Give the extent of all Plasmodium malariae-infected red blood cells.
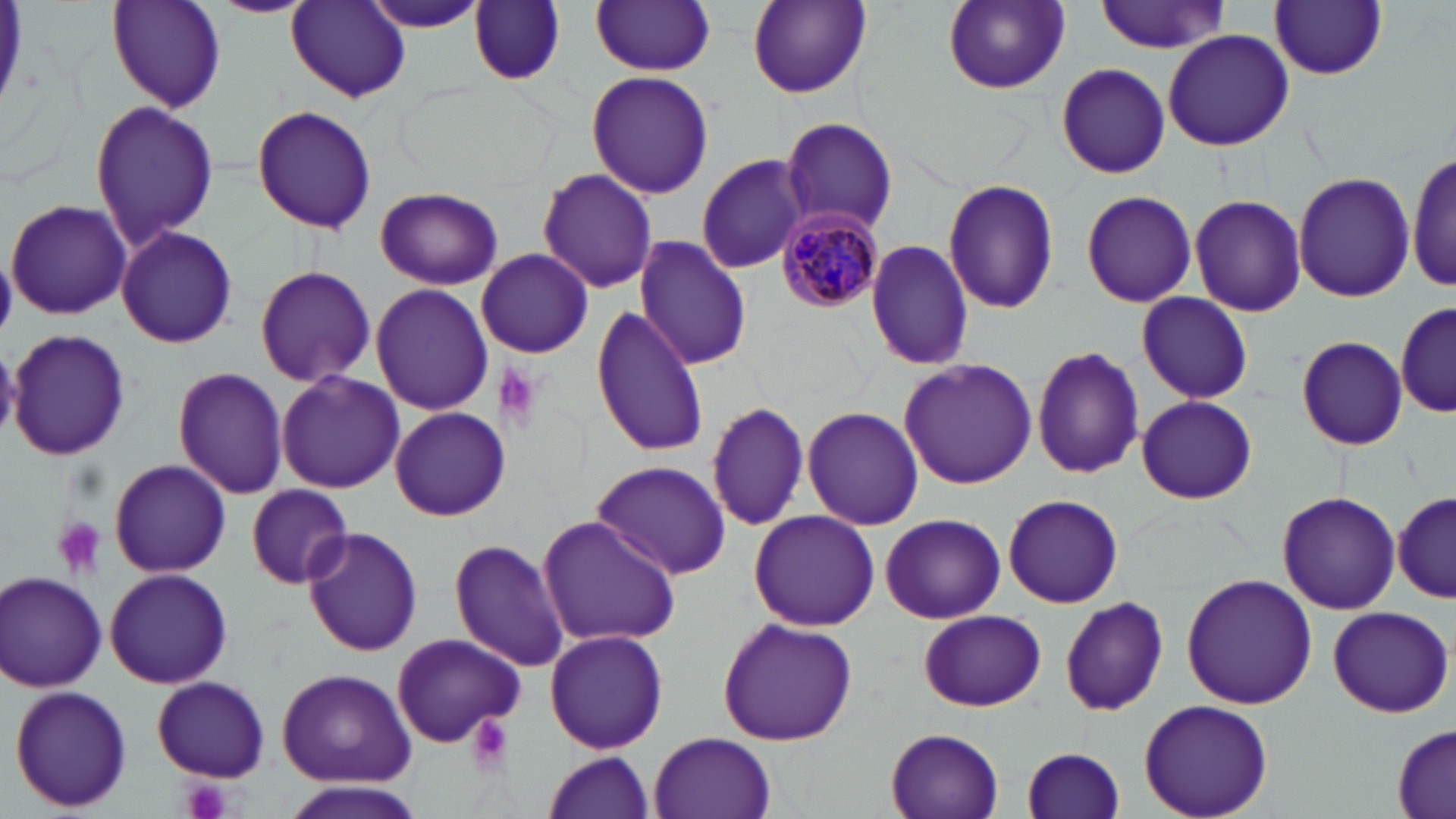
Approximate bounding boxes as [x1, y1, x2, y2] in pixels.
Plasmodium malariae-infected red blood cells: [774, 203, 886, 314].

Platelet locations: [491, 365, 545, 431], [52, 518, 106, 579], [466, 715, 513, 777], [179, 777, 232, 819]. Uninfected red blood cell locations: [207, 0, 317, 18], [942, 0, 1069, 93], [107, 1, 226, 112], [285, 1, 410, 104], [358, 1, 489, 33], [468, 1, 566, 86], [746, 1, 870, 98], [1093, 1, 1232, 54], [591, 2, 718, 75], [1271, 2, 1388, 80], [1162, 29, 1294, 153], [1057, 63, 1170, 177], [586, 68, 714, 199], [88, 99, 219, 252], [252, 104, 376, 235], [779, 116, 898, 235], [1408, 150, 1456, 296], [696, 154, 810, 272], [536, 168, 658, 293], [1294, 171, 1415, 302], [942, 178, 1059, 315], [374, 186, 503, 291], [1079, 190, 1197, 308], [1188, 194, 1307, 317], [5, 198, 130, 319], [115, 225, 237, 349], [632, 236, 752, 369], [863, 238, 975, 372], [477, 248, 592, 359], [254, 264, 376, 389], [370, 282, 492, 416], [1135, 292, 1255, 404], [1395, 297, 1453, 419], [591, 305, 709, 458], [7, 327, 131, 463], [1295, 335, 1409, 451], [1031, 344, 1144, 481], [898, 357, 1037, 490], [171, 367, 289, 501], [274, 371, 404, 495], [1132, 394, 1260, 503], [706, 400, 809, 533], [388, 407, 511, 521], [802, 407, 925, 531], [590, 459, 732, 580], [109, 460, 230, 577], [244, 484, 354, 587], [1392, 488, 1454, 604], [1276, 491, 1400, 614], [1002, 492, 1125, 608], [748, 509, 880, 631], [879, 512, 1007, 625], [537, 513, 682, 648], [300, 527, 425, 657], [448, 537, 572, 673], [105, 568, 232, 688], [1, 571, 108, 692], [1180, 572, 1317, 709], [1060, 595, 1169, 716], [1326, 606, 1453, 718], [917, 609, 1046, 711], [717, 617, 857, 747], [543, 628, 668, 755], [391, 632, 525, 747], [278, 667, 414, 787], [152, 675, 271, 782], [9, 684, 133, 814], [1138, 699, 1274, 819], [1391, 719, 1456, 819], [881, 727, 1005, 819], [650, 732, 774, 819], [1020, 746, 1126, 819], [541, 750, 655, 819], [283, 781, 422, 819]. Slide-level diagnosis: Plasmodium malariae. May-Grünwald-Giemsa-stained preparation. Image is 1456×819 pixels. Optical microscopy. Single field of view. Captured at 1000x magnification. Thin blood film.